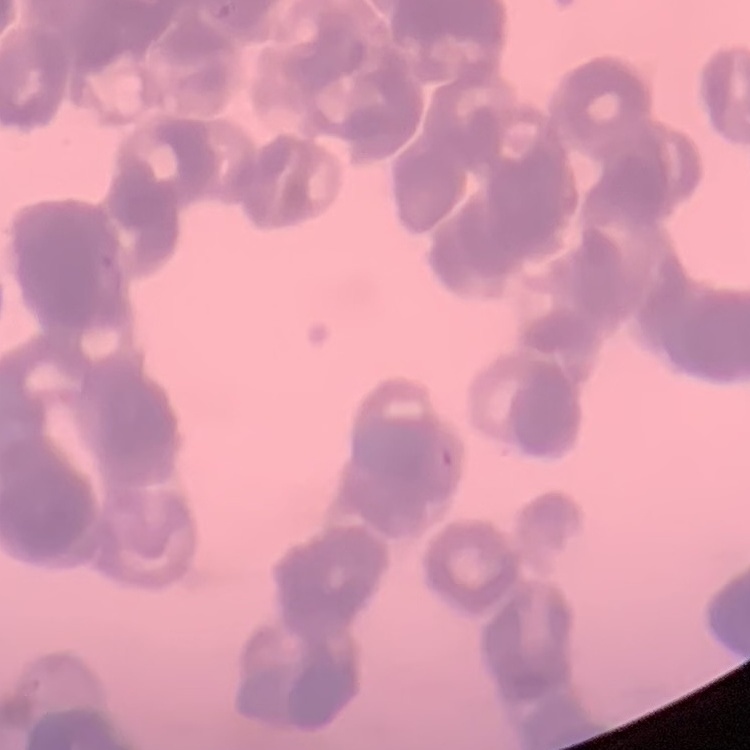
erythrocyte morphology = rouleaux formation
preparation = thin blood smear
image type = one tile cut from a larger photomicrograph
stain = Field's or Giemsa